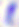
{
  "magnification": "400x",
  "identification": "Toxoplasma gondii",
  "modality": "micrograph"
}